Assess the morphology of the red blood cells.
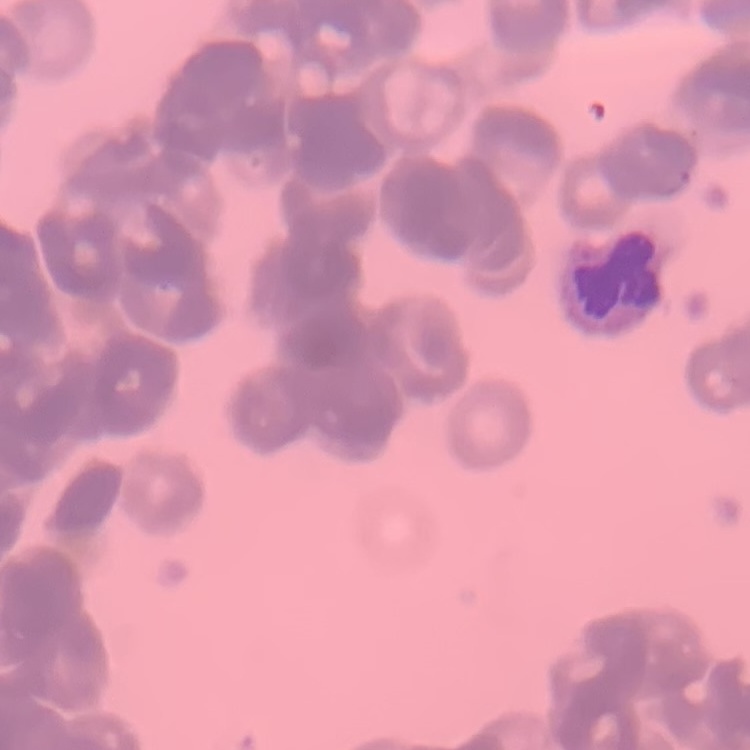
Rouleaux formation.

Field's or Giemsa stain. Thin peripheral smear. Square crop of a larger photomicrograph.